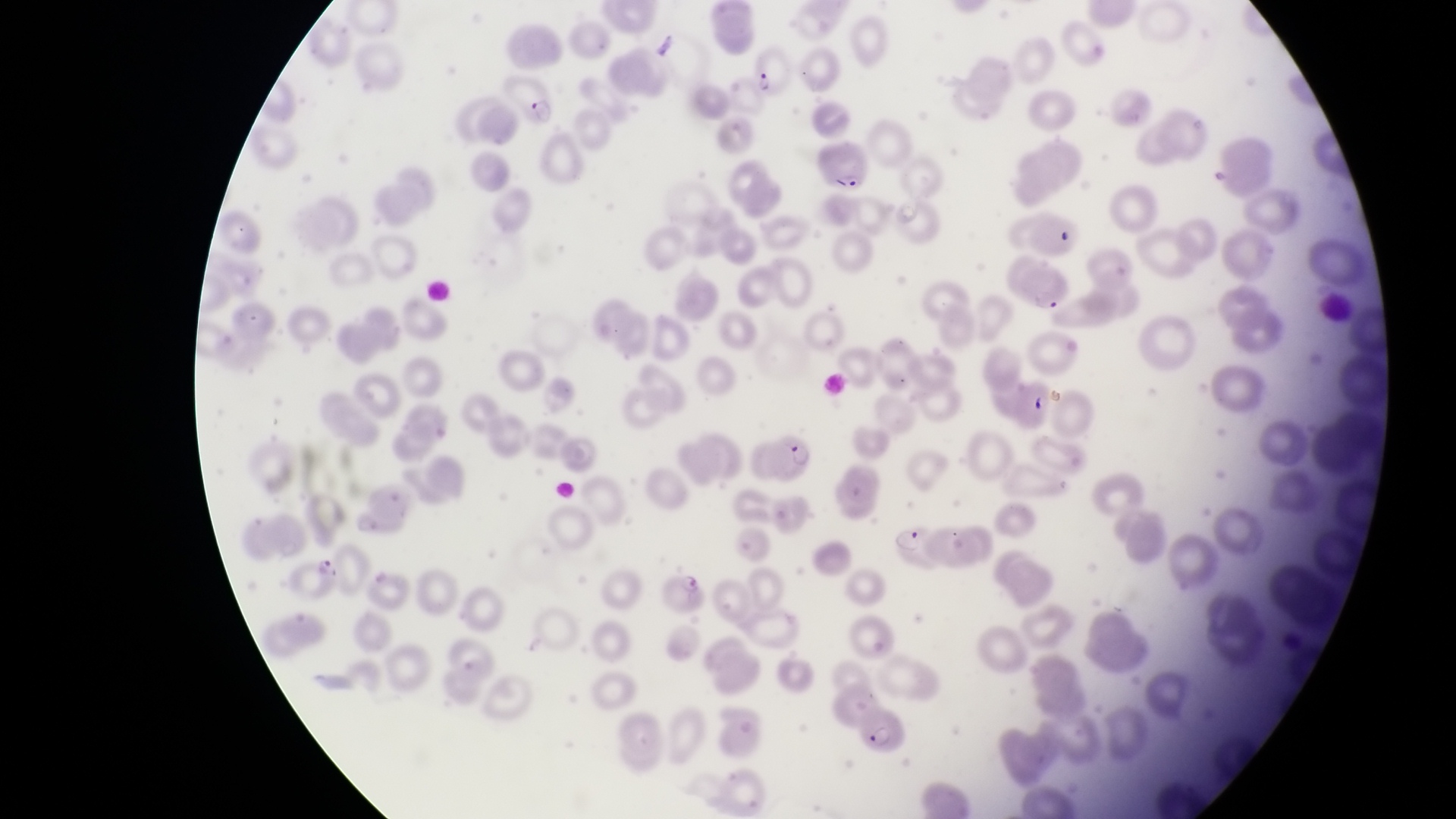

country: Uganda
magnification: 1000x
field_of_view: single
image_size: 1456×819 pixels
capture: smartphone photograph through the eyepiece of an Olympus CX-23 microscope
parasitised_red_blood_cell_locations: 'approximate bounding boxes as [left, top, right, bottom] in pixels: [750, 49, 789, 102], [502, 72, 557, 127], [817, 143, 872, 193], [763, 428, 821, 481], [888, 519, 934, 569], [858, 704, 914, 760]'
preparation: thin blood smear